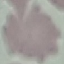
result = no malaria parasites seen
stain = Giemsa
capture = smartphone through the microscope eyepiece
image type = automatically extracted cell patch, resized to 64 × 64 pixels
preparation = thin smear